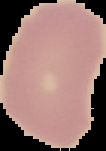
Summary:
  - Image size: 106×151 pixels
  - Image type: segmented cell region with the area outside set to black
  - Malaria status: uninfected
  - Preparation: thin blood smear